Assess this cell for malaria.
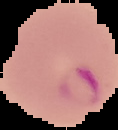

Parasitized.

Summary:
  - Preparation: thin blood film
  - Image type: segmented cell region on a black background
  - Image size: 118×130 pixels